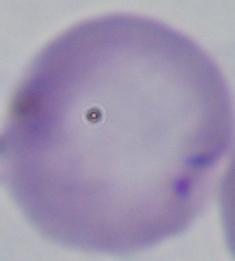
magnification: 1000x
modality: photomicrograph
identification: Babesia